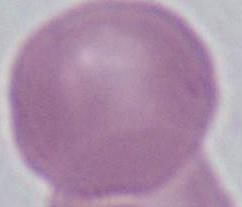
Summary:
  - Magnification: 1000x
  - Identification: red blood cell
  - Modality: micrograph